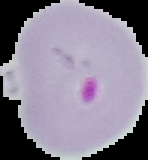
Summary:
  - Image size: 148×160 pixels
  - Image type: segmented cell region on a black background
  - Preparation: thin blood film
  - Result: Plasmodium parasites detected